State the blood parasite species.
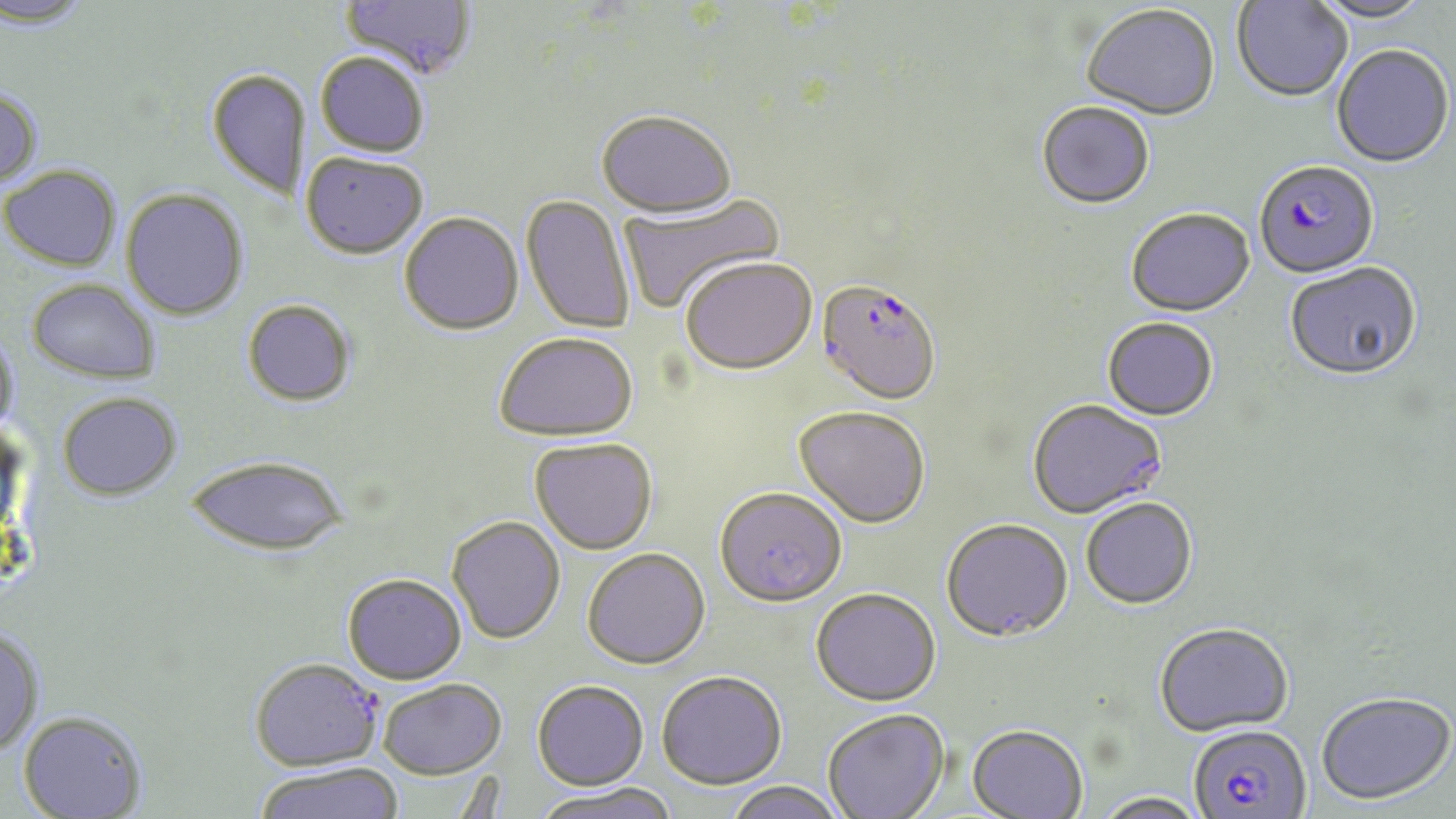
Plasmodium falciparum.

Approximate bounding boxes as named x1/y1/x2/y2 corners in pixels. Uninfected red blood cell locations: (x1=0, y1=0, x2=94, y2=29), (x1=340, y1=0, x2=477, y2=82), (x1=1309, y1=0, x2=1434, y2=25), (x1=1232, y1=1, x2=1352, y2=104), (x1=1081, y1=6, x2=1221, y2=122), (x1=1332, y1=46, x2=1454, y2=169), (x1=315, y1=54, x2=428, y2=158), (x1=207, y1=68, x2=311, y2=201), (x1=0, y1=86, x2=44, y2=191), (x1=1036, y1=103, x2=1155, y2=212), (x1=597, y1=112, x2=736, y2=220), (x1=300, y1=153, x2=428, y2=261), (x1=1, y1=164, x2=122, y2=271), (x1=120, y1=188, x2=248, y2=320), (x1=618, y1=192, x2=785, y2=315), (x1=520, y1=195, x2=635, y2=335), (x1=1126, y1=210, x2=1255, y2=319), (x1=399, y1=213, x2=524, y2=337), (x1=681, y1=257, x2=817, y2=377), (x1=1285, y1=263, x2=1423, y2=384), (x1=26, y1=278, x2=161, y2=384), (x1=241, y1=299, x2=356, y2=407), (x1=1102, y1=319, x2=1218, y2=422), (x1=0, y1=327, x2=20, y2=440), (x1=494, y1=333, x2=639, y2=442), (x1=57, y1=392, x2=182, y2=500), (x1=1027, y1=400, x2=1168, y2=521), (x1=794, y1=407, x2=931, y2=530), (x1=529, y1=438, x2=658, y2=554), (x1=188, y1=455, x2=348, y2=557), (x1=714, y1=488, x2=847, y2=608), (x1=1081, y1=500, x2=1197, y2=611), (x1=447, y1=516, x2=566, y2=644), (x1=941, y1=521, x2=1074, y2=645), (x1=582, y1=547, x2=710, y2=669), (x1=341, y1=573, x2=467, y2=684), (x1=810, y1=589, x2=941, y2=708), (x1=1154, y1=624, x2=1294, y2=738), (x1=0, y1=626, x2=45, y2=755), (x1=656, y1=670, x2=787, y2=790), (x1=379, y1=679, x2=507, y2=779), (x1=532, y1=679, x2=649, y2=790), (x1=1316, y1=692, x2=1455, y2=806), (x1=823, y1=709, x2=950, y2=819), (x1=18, y1=711, x2=148, y2=818), (x1=967, y1=726, x2=1088, y2=819), (x1=252, y1=763, x2=405, y2=819), (x1=723, y1=780, x2=847, y2=819), (x1=531, y1=782, x2=678, y2=819), (x1=1091, y1=792, x2=1210, y2=819). Plasmodium falciparum-infected red blood cell locations: (x1=1253, y1=162, x2=1379, y2=281), (x1=816, y1=281, x2=941, y2=408), (x1=248, y1=658, x2=381, y2=771), (x1=1189, y1=725, x2=1312, y2=819). Thin blood film. Single field of view. May-Grünwald-Giemsa stain. Light microscopy. 1000x magnification. Image is 1456×819 pixels.